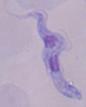

magnification = 1000x
modality = micrograph
identification = trypanosome